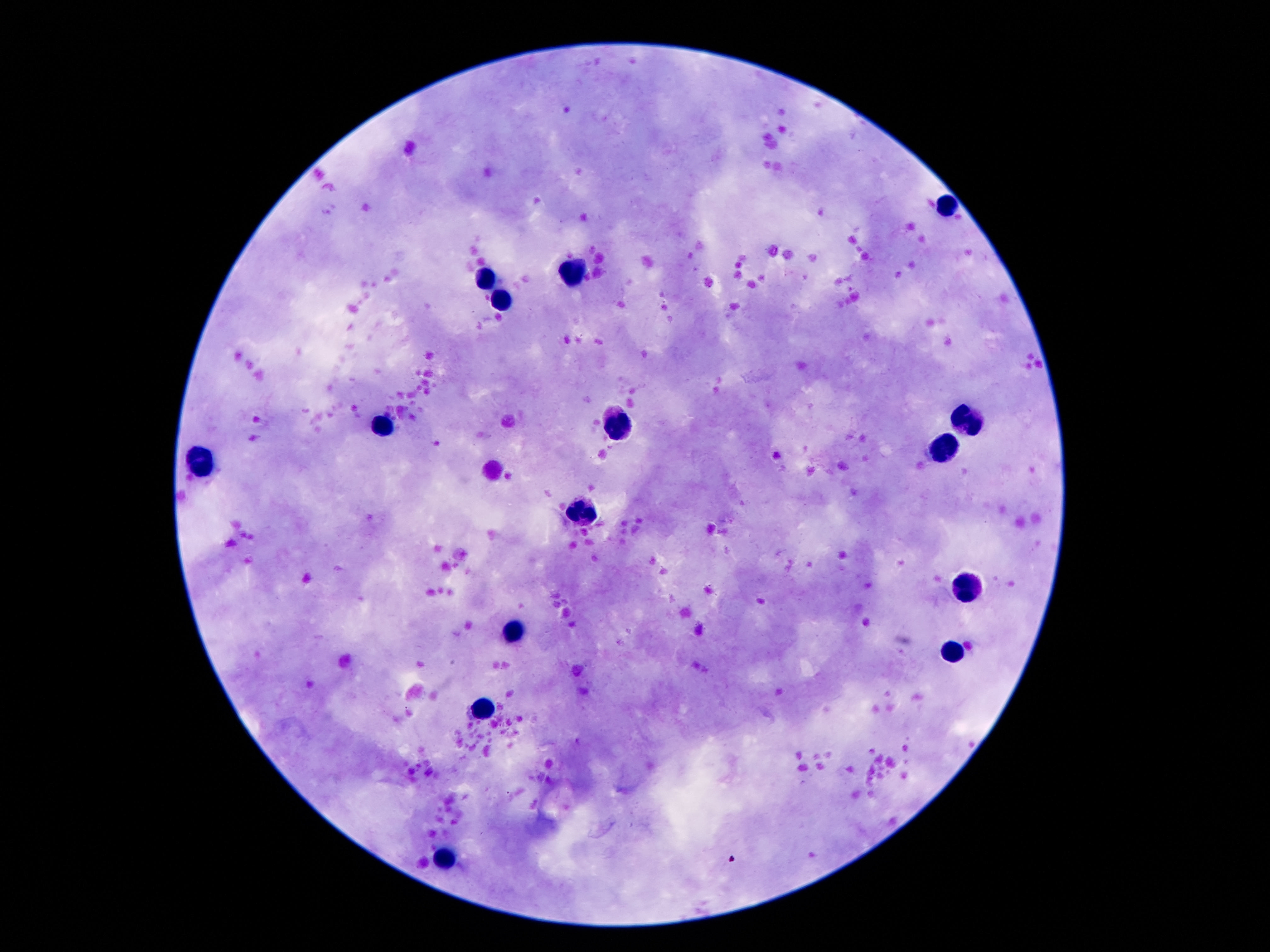
Approximate centers as (x, y) in pixels.
Summary:
  - Leukocyte locations: (947, 205), (578, 271), (482, 276), (505, 300), (973, 418), (615, 422), (385, 425), (947, 444), (202, 461), (581, 511), (962, 586), (516, 633), (955, 653), (484, 707), (445, 854)
  - Magnification: 100x
  - Capture: smartphone camera through the microscope eyepiece
  - Stain: Giemsa
  - Image size: 1270×952 pixels
  - Field of view: one from this slide
  - Preparation: thick blood smear
  - Patient malaria status: not infected